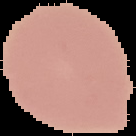
preparation = thin blood film
image size = 136×136 pixels
result = negative for Plasmodium parasites
image type = cell region segmented out of the field of view; surrounding area masked to black